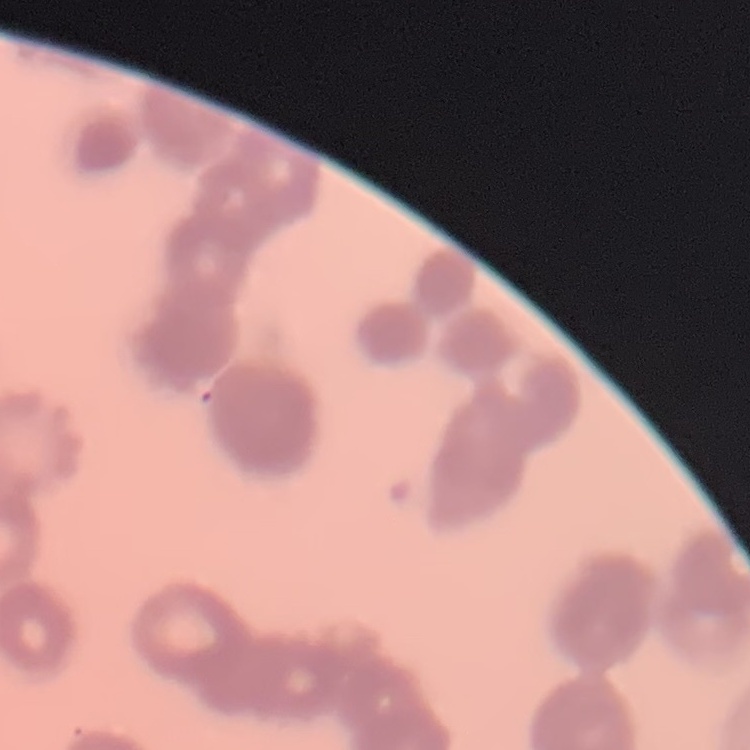

erythrocyte_morphology: rouleaux formation
preparation: thin blood film
stain: Field's or Giemsa
image_type: square crop of a larger photomicrograph